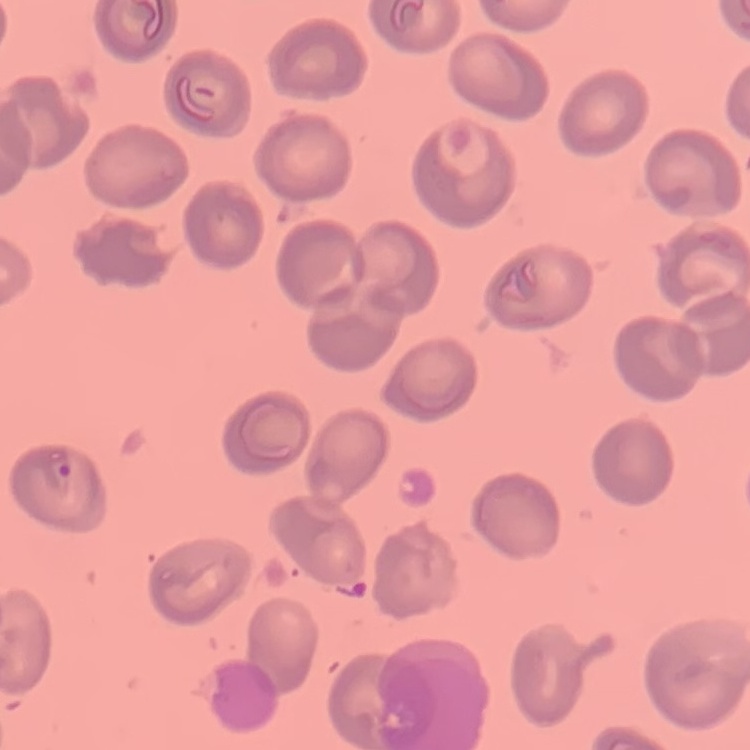

{
  "erythrocyte_morphology": "no rouleaux formation",
  "image_type": "square crop of a larger photomicrograph",
  "stain": "Field's or Giemsa",
  "preparation": "thin blood smear"
}